Classify this cell by malaria status.
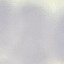
It is uninfected.

capture = smartphone camera at the microscope eyepiece
stain = Giemsa
preparation = thin blood film
image type = automatically extracted cell patch, resized to 64 × 64 pixels